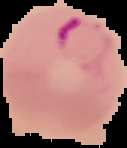

{
  "malaria_status": "parasitized",
  "image_type": "segmented cell region with the area outside set to black",
  "preparation": "thin blood film",
  "image_size": "127×148 pixels"
}